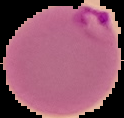
Summary:
  - Image size: 124×118 pixels
  - Image type: segmented cell region with the area outside set to black
  - Preparation: thin blood film
  - Malaria status: parasitized